Give the extent of all Plasmodium vivax-infected red blood cells.
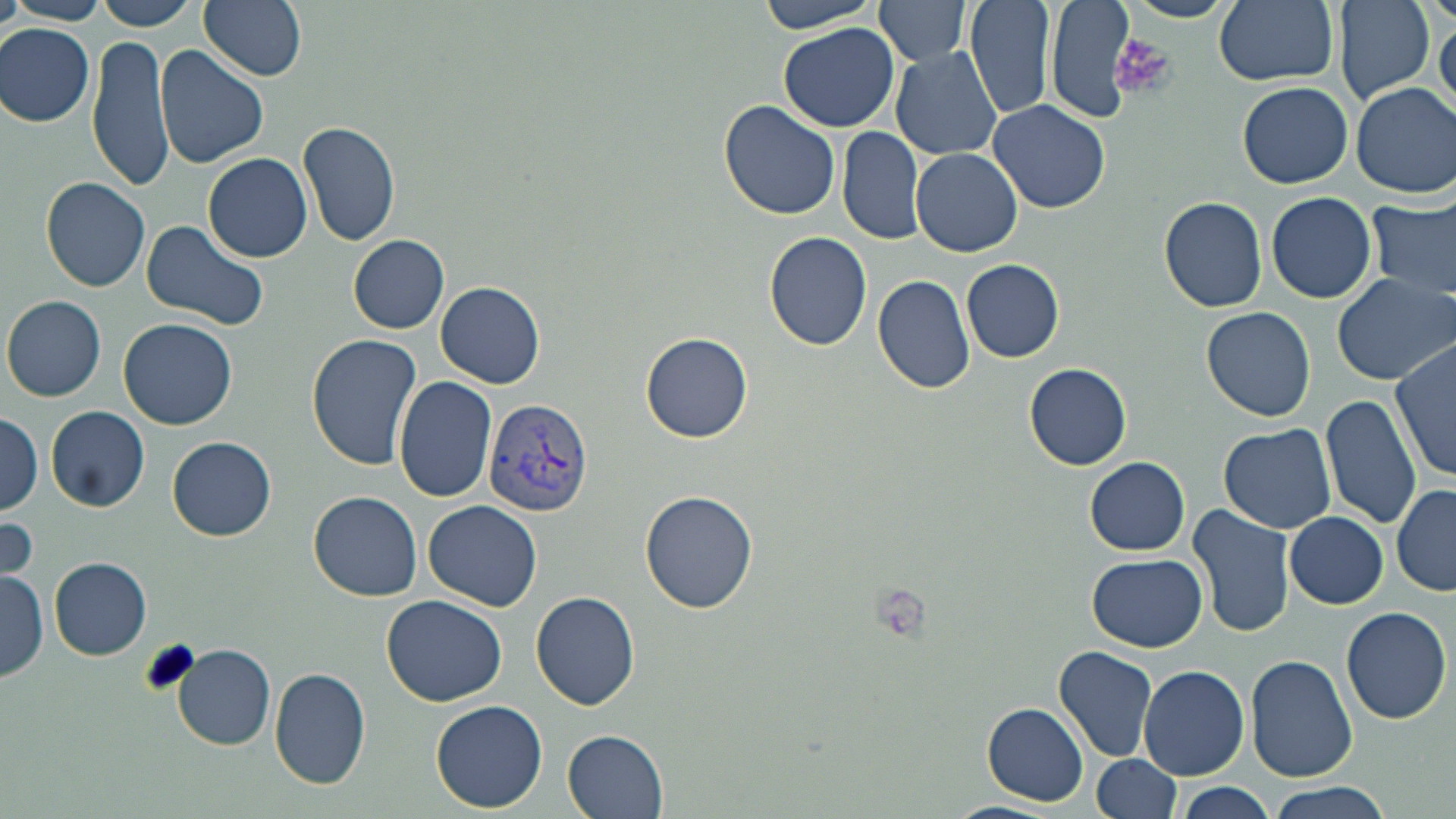
Approximate bounding boxes as (x1,y1)-(x2,y2) corner pairs in pixels.
Plasmodium vivax-infected red blood cells: (484,399)-(594,516).

Platelet locations: (1114,32)-(1175,103), (138,639)-(200,699). Uninfected red blood cell locations: (0,0)-(25,41), (91,0)-(202,30), (199,0)-(307,81), (755,0)-(889,34), (874,0)-(975,66), (966,0)-(1054,122), (1043,0)-(1139,124), (1124,0)-(1234,23), (1214,0)-(1337,87), (2,1)-(112,25), (1335,1)-(1435,102), (1430,11)-(1456,113), (778,22)-(900,132), (1,23)-(96,126), (89,35)-(172,189), (156,44)-(268,169), (892,46)-(1003,161), (1239,81)-(1353,188), (1352,83)-(1455,198), (719,100)-(841,220), (986,100)-(1112,215), (298,121)-(402,247), (838,125)-(925,245), (911,147)-(1024,256), (204,152)-(313,261), (42,177)-(151,292), (1267,191)-(1376,305), (1160,195)-(1268,313), (1367,195)-(1455,303), (141,219)-(270,331), (764,231)-(874,352), (350,235)-(449,333), (962,259)-(1065,362), (1330,271)-(1456,386), (872,274)-(975,394), (436,282)-(545,388), (3,294)-(106,401), (1202,307)-(1317,422), (119,317)-(238,430), (641,331)-(754,442), (308,333)-(424,469), (1392,339)-(1455,483), (1025,362)-(1132,470), (394,375)-(500,502), (1321,393)-(1422,530), (47,405)-(149,511), (0,412)-(45,514), (1217,423)-(1337,535), (167,436)-(277,541), (1085,458)-(1189,555), (1392,484)-(1456,597), (640,488)-(759,613), (308,491)-(423,601), (423,500)-(543,612), (1188,504)-(1299,638), (0,513)-(39,592), (1285,513)-(1388,608), (1089,554)-(1207,650), (50,558)-(151,659), (0,569)-(49,683), (531,591)-(642,710), (382,595)-(510,708), (1342,607)-(1451,725), (172,644)-(277,749), (1054,645)-(1159,763), (1246,654)-(1356,783), (1139,665)-(1248,781), (271,666)-(370,789), (431,699)-(548,812), (982,703)-(1089,804), (564,730)-(671,818), (1093,756)-(1180,817), (1175,783)-(1279,817), (1265,784)-(1395,817). Slide-level diagnosis: Plasmodium vivax. 1000x magnification. Image is 1456×819 pixels. Optical microscopy. May-Grünwald-Giemsa-stained preparation. Thin blood smear. One field of a larger specimen.